Name the parasite shown.
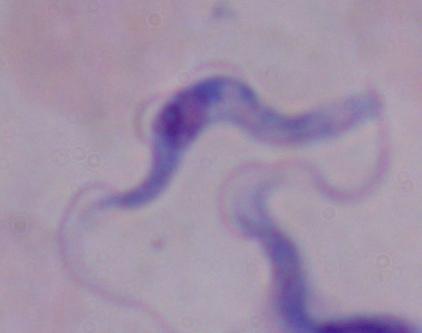

A trypanosome.

Captured at 1000x magnification. Micrograph.